Name the cell type shown.
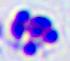

A leukocyte.

Summary:
  - Modality: photomicrograph
  - Magnification: 400x